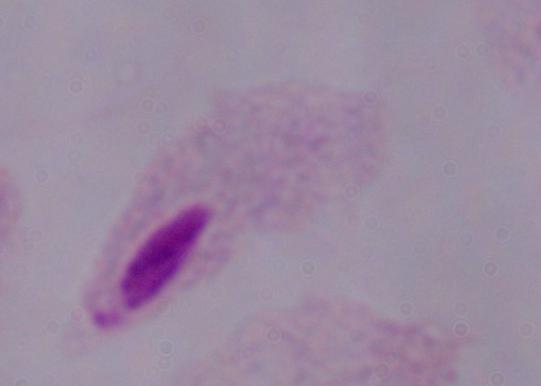

Summary:
  - Identification: trichomonad
  - Modality: micrograph
  - Magnification: 1000x